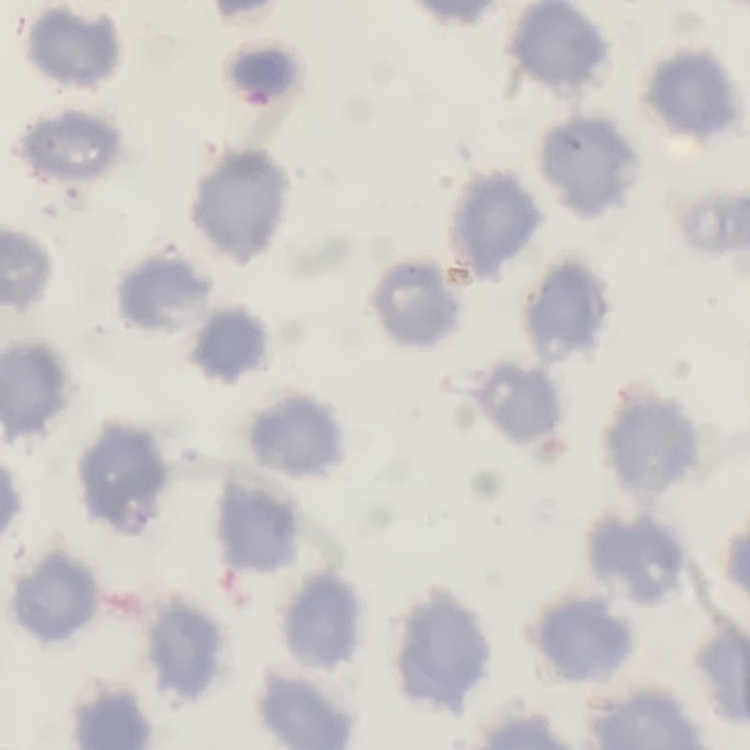
red_blood_cell_morphology: no rouleaux formation
stain: Field's or Giemsa
image_type: square crop of a larger photomicrograph
preparation: thin blood film